Assess this cell for malaria.
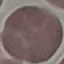
It is uninfected.

Summary:
  - Image type: automatically extracted cell patch, resized to 64 × 64 pixels
  - Preparation: thin smear
  - Capture: smartphone through the microscope eyepiece
  - Stain: Giemsa